Locate every Plasmodium vivax-infected red blood cell.
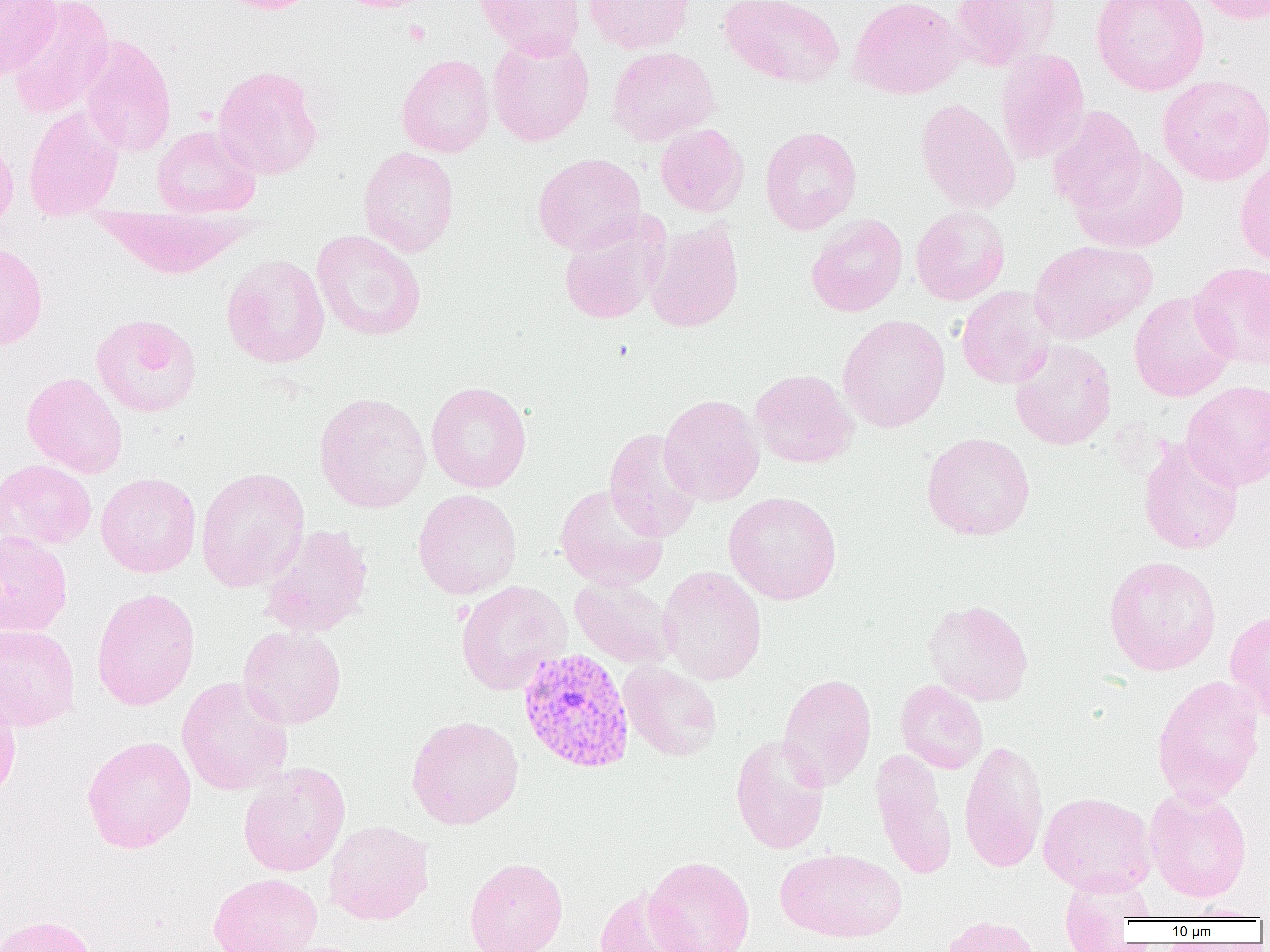

Approximate bounding boxes as named x1/y1/x2/y2 corners in pixels.
Plasmodium vivax-infected red blood cells: (x1=517, y1=648, x2=635, y2=773).

Summary:
  - Uninfected red blood cell locations: (x1=0, y1=0, x2=62, y2=79), (x1=6, y1=0, x2=114, y2=119), (x1=213, y1=0, x2=321, y2=14), (x1=337, y1=0, x2=434, y2=13), (x1=474, y1=0, x2=585, y2=58), (x1=583, y1=0, x2=695, y2=54), (x1=719, y1=0, x2=845, y2=88), (x1=847, y1=0, x2=968, y2=99), (x1=950, y1=0, x2=1062, y2=72), (x1=1091, y1=0, x2=1209, y2=95), (x1=1194, y1=0, x2=1270, y2=24), (x1=487, y1=32, x2=595, y2=146), (x1=79, y1=34, x2=177, y2=157), (x1=607, y1=46, x2=720, y2=146), (x1=995, y1=48, x2=1090, y2=164), (x1=397, y1=54, x2=495, y2=157), (x1=213, y1=65, x2=324, y2=180), (x1=1157, y1=75, x2=1270, y2=186), (x1=915, y1=99, x2=1020, y2=214), (x1=1047, y1=105, x2=1147, y2=216), (x1=23, y1=107, x2=123, y2=220), (x1=655, y1=123, x2=748, y2=216), (x1=152, y1=125, x2=261, y2=218), (x1=760, y1=126, x2=862, y2=235), (x1=0, y1=133, x2=19, y2=233), (x1=358, y1=147, x2=459, y2=257), (x1=1073, y1=148, x2=1190, y2=253), (x1=533, y1=153, x2=646, y2=256), (x1=1235, y1=156, x2=1270, y2=267), (x1=91, y1=206, x2=252, y2=278), (x1=911, y1=206, x2=1010, y2=305), (x1=805, y1=213, x2=908, y2=316), (x1=558, y1=219, x2=664, y2=325), (x1=644, y1=220, x2=745, y2=333), (x1=312, y1=230, x2=426, y2=341), (x1=1029, y1=240, x2=1157, y2=344), (x1=0, y1=242, x2=48, y2=350), (x1=221, y1=253, x2=330, y2=369), (x1=1189, y1=261, x2=1270, y2=369), (x1=956, y1=286, x2=1056, y2=389), (x1=1129, y1=291, x2=1237, y2=402), (x1=90, y1=313, x2=202, y2=417), (x1=837, y1=314, x2=950, y2=433), (x1=1010, y1=340, x2=1117, y2=450), (x1=749, y1=369, x2=859, y2=469), (x1=22, y1=372, x2=128, y2=478), (x1=1181, y1=380, x2=1270, y2=492), (x1=425, y1=381, x2=532, y2=493), (x1=314, y1=392, x2=432, y2=513), (x1=658, y1=394, x2=764, y2=506), (x1=604, y1=428, x2=701, y2=542), (x1=921, y1=432, x2=1036, y2=541), (x1=1138, y1=437, x2=1243, y2=556), (x1=0, y1=458, x2=96, y2=550), (x1=196, y1=466, x2=309, y2=592), (x1=95, y1=472, x2=202, y2=577), (x1=554, y1=484, x2=669, y2=591), (x1=413, y1=488, x2=522, y2=599), (x1=723, y1=491, x2=843, y2=605), (x1=259, y1=523, x2=374, y2=638), (x1=0, y1=531, x2=73, y2=637), (x1=1103, y1=555, x2=1222, y2=676), (x1=658, y1=566, x2=767, y2=685), (x1=569, y1=576, x2=677, y2=670), (x1=455, y1=580, x2=571, y2=695), (x1=91, y1=588, x2=200, y2=711), (x1=922, y1=599, x2=1034, y2=705), (x1=1224, y1=609, x2=1270, y2=725), (x1=0, y1=623, x2=81, y2=732), (x1=238, y1=626, x2=347, y2=729), (x1=618, y1=661, x2=722, y2=761), (x1=778, y1=673, x2=876, y2=791), (x1=1152, y1=674, x2=1265, y2=806), (x1=176, y1=676, x2=293, y2=796), (x1=896, y1=680, x2=988, y2=774), (x1=0, y1=689, x2=21, y2=804), (x1=406, y1=715, x2=524, y2=829), (x1=730, y1=734, x2=830, y2=855), (x1=82, y1=736, x2=197, y2=854), (x1=959, y1=738, x2=1049, y2=874), (x1=870, y1=748, x2=956, y2=879), (x1=238, y1=762, x2=351, y2=877), (x1=1144, y1=786, x2=1252, y2=903), (x1=1038, y1=792, x2=1157, y2=895), (x1=324, y1=820, x2=434, y2=925), (x1=776, y1=848, x2=906, y2=942), (x1=643, y1=856, x2=755, y2=952), (x1=464, y1=858, x2=567, y2=952), (x1=208, y1=872, x2=323, y2=952), (x1=1058, y1=872, x2=1154, y2=951), (x1=593, y1=887, x2=698, y2=952), (x1=1176, y1=904, x2=1266, y2=921), (x1=0, y1=914, x2=97, y2=952), (x1=939, y1=915, x2=1044, y2=952)
  - Slide-level diagnosis: Plasmodium vivax
  - Image size: 1270×952 pixels
  - Magnification: 1000x
  - Field of view: one of a larger specimen
  - Preparation: thin blood smear
  - Modality: optical microscopy